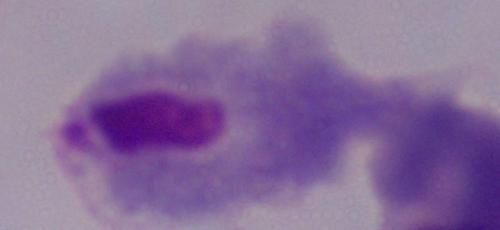

magnification = 1000x
identification = trichomonad
modality = micrograph